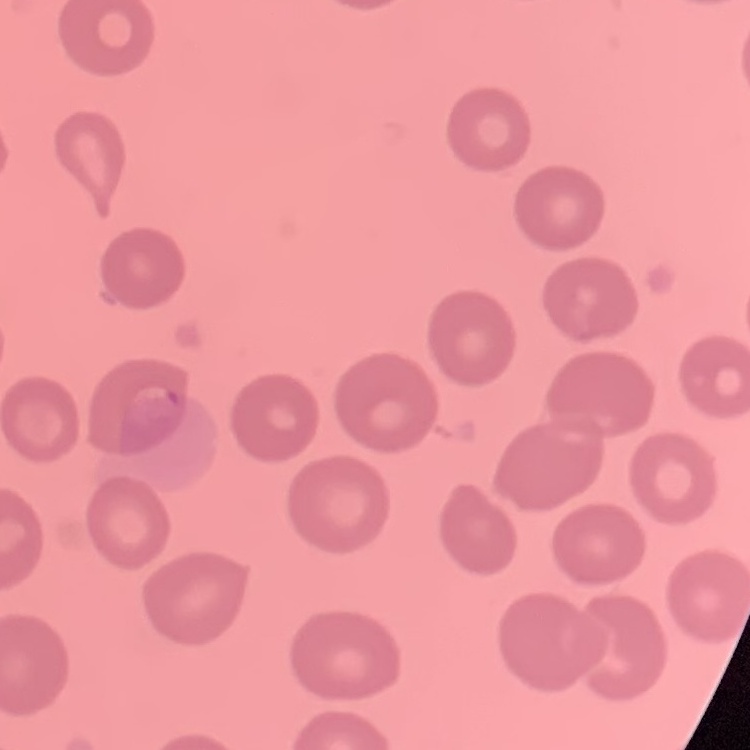

Summary:
  - Erythrocyte morphology: no rouleaux formation
  - Image type: one tile cut from a larger photomicrograph
  - Preparation: thin blood smear
  - Stain: Field's or Giemsa